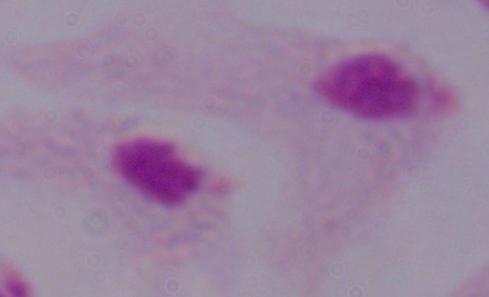

Summary:
  - Identification: trichomonad
  - Magnification: 1000x
  - Modality: photomicrograph